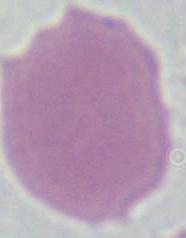

Summary:
  - Modality: micrograph
  - Identification: erythrocyte
  - Magnification: 1000x